Report the malaria status of this cell.
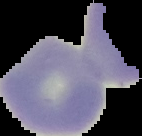
It is uninfected.

image size = 142×136 pixels
preparation = thin blood smear
image type = segmented cell region on a black background